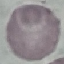
result = negative for malaria parasites
capture = smartphone camera at the microscope eyepiece
image type = cell patch, automatically extracted from a larger field of view and resized to 64 × 64 pixels
preparation = thin blood smear
stain = Giemsa